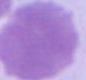

Summary:
  - Identification: red blood cell
  - Modality: photomicrograph
  - Magnification: 1000x